Outline each blood parasite and name the species.
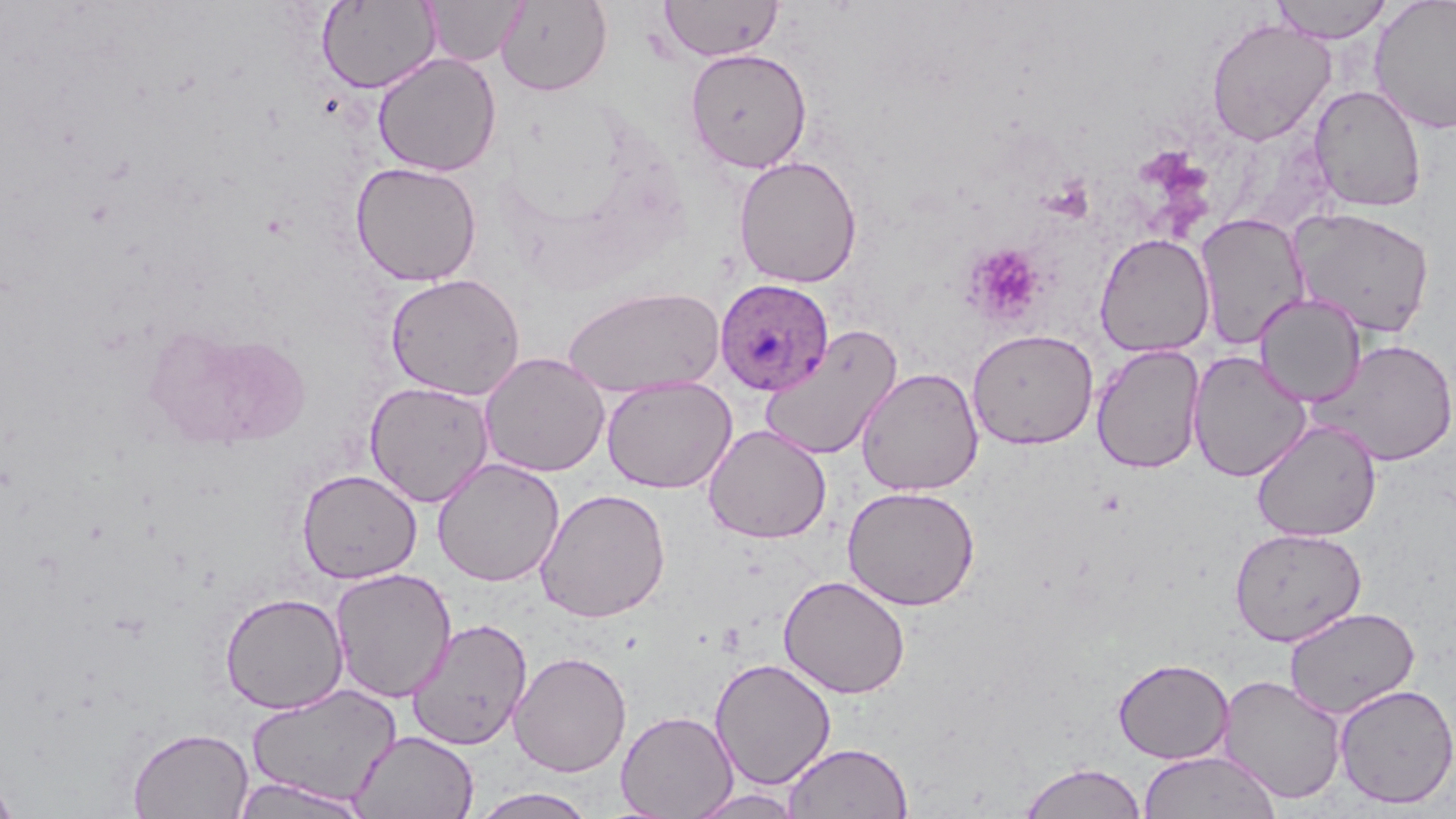
Approximate bounding boxes as [x1, y1, x2, y2] in pixels.
Plasmodium ovale-infected red blood cells: [714, 277, 834, 396].
No Plasmodium falciparum, Plasmodium malariae, Plasmodium vivax, Babesia divergens, or Trypanosoma brucei observed.

Summary:
  - Platelet locations: [964, 243, 1047, 325]
  - Uninfected red blood cell locations: [659, 0, 784, 62], [1269, 0, 1393, 43], [1369, 0, 1456, 135], [317, 1, 440, 93], [426, 1, 526, 66], [496, 1, 612, 96], [1205, 17, 1336, 146], [685, 47, 812, 173], [372, 52, 501, 177], [1309, 84, 1427, 213], [733, 155, 862, 288], [350, 161, 483, 287], [1287, 207, 1436, 339], [1195, 213, 1310, 350], [1095, 233, 1215, 358], [385, 272, 525, 400], [562, 285, 725, 398], [1253, 293, 1366, 407], [144, 323, 310, 449], [759, 325, 902, 461], [967, 328, 1099, 450], [1310, 338, 1456, 467], [1091, 344, 1206, 474], [1188, 350, 1311, 482], [480, 352, 610, 477], [856, 366, 984, 496], [601, 376, 736, 493], [365, 381, 495, 507], [1251, 420, 1382, 542], [703, 425, 832, 544], [431, 457, 565, 587], [296, 468, 422, 583], [842, 485, 980, 611], [535, 487, 671, 623], [1229, 527, 1367, 646], [329, 567, 457, 703], [778, 575, 911, 699], [219, 591, 349, 714], [1284, 606, 1420, 719], [406, 617, 533, 750], [509, 651, 632, 778], [709, 657, 837, 790], [1112, 657, 1234, 764], [1218, 674, 1348, 804], [245, 682, 401, 807], [1333, 683, 1456, 809], [616, 710, 738, 819], [127, 726, 254, 819], [351, 730, 479, 819], [783, 742, 914, 818], [1138, 749, 1282, 819], [1017, 761, 1148, 819], [0, 772, 19, 819], [231, 776, 368, 818], [469, 787, 598, 818], [686, 788, 805, 819]
  - Slide-level diagnosis: Plasmodium ovale
  - Modality: optical microscopy
  - Image size: 1456×819 pixels
  - Field of view: one of a larger specimen
  - Magnification: 1000x
  - Stain: May-Grünwald-Giemsa
  - Preparation: thin blood smear